State which parasite is depicted.
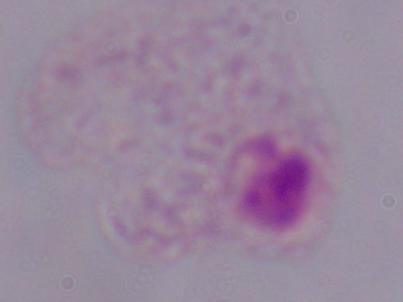

A trichomonad.

{
  "magnification": "1000x",
  "modality": "photomicrograph"
}